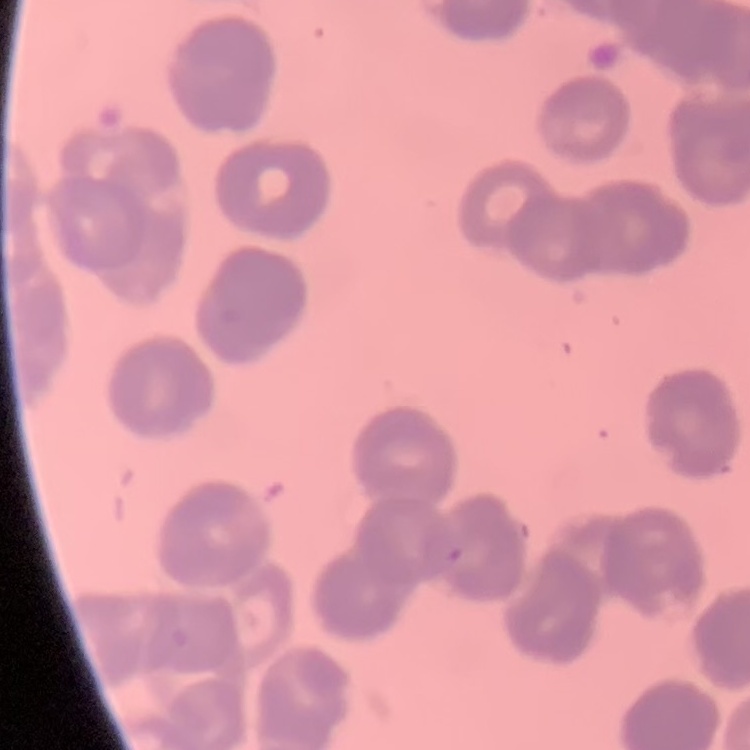

{
  "erythrocyte_morphology": "rouleaux formation",
  "preparation": "thin blood film",
  "image_type": "one tile cut from a larger photomicrograph",
  "stain": "Field's or Giemsa"
}